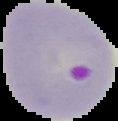
image_type: segmented cell region with the area outside set to black
malaria_status: parasitized
image_size: 118×121 pixels
preparation: thin blood film